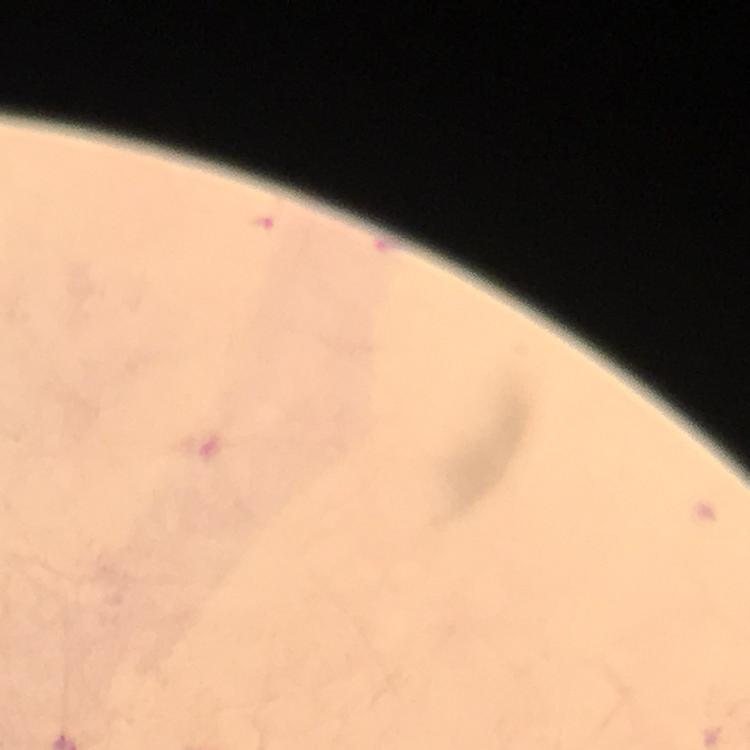
magnification = 100x
preparation = thick blood film
stain = Giemsa
Plasmodium parasite locations = approximate object centers, in pixels from the top-left corner: (x=259, y=224)
capture = smartphone mounted on the microscope
context = from a malaria diagnostic workup
image size = 750×750 pixels
cropped from = a single field of view
immersion oil = used